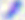
modality = micrograph
magnification = 400x
identification = Toxoplasma gondii